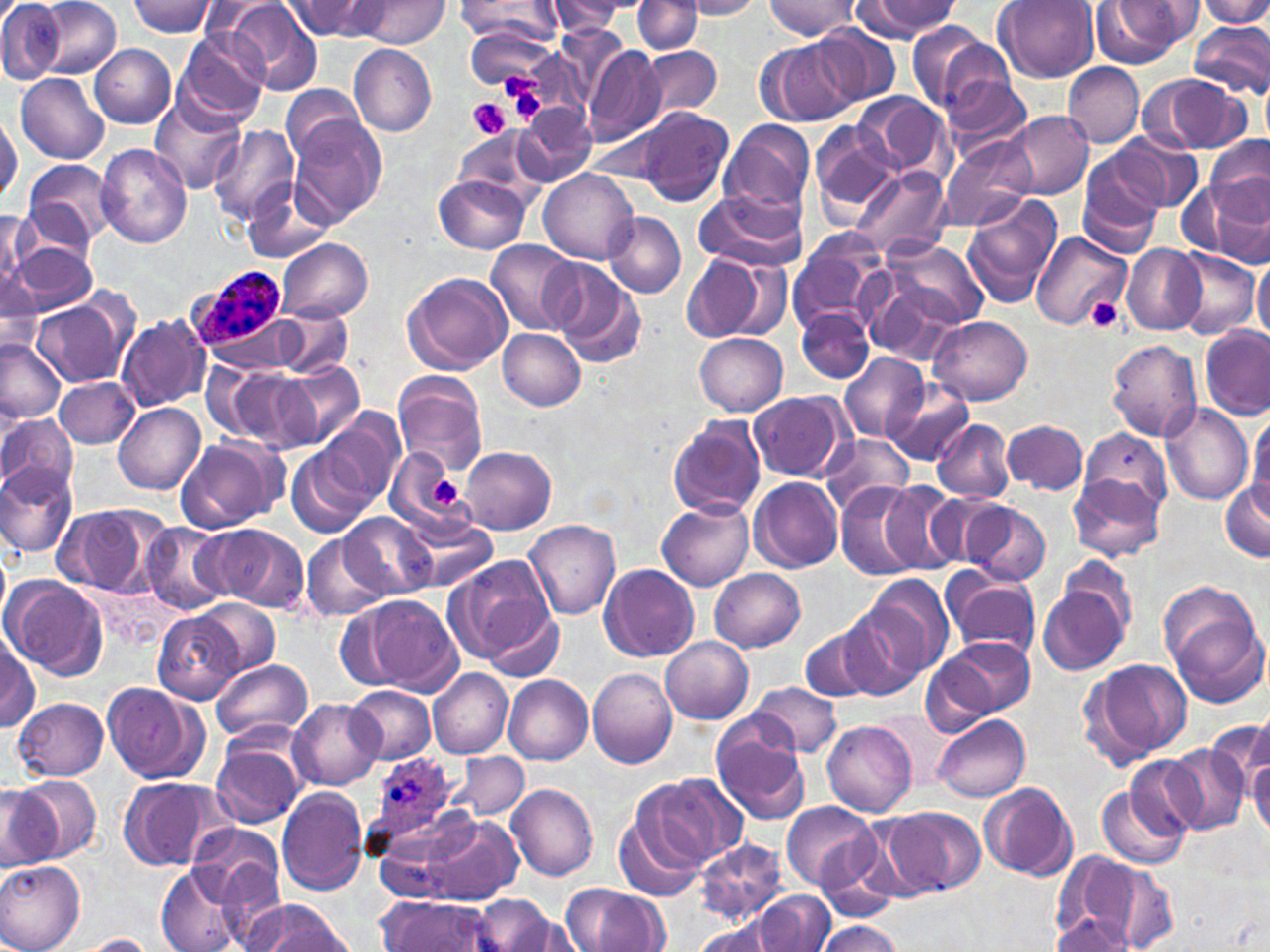 Approximate bounding boxes as named x1/y1/x2/y2 corners in pixels. Plasmodium ovale-infected red blood cell locations: (x1=191, y1=267, x2=287, y2=349), (x1=378, y1=750, x2=462, y2=838). Uninfected red blood cell locations: (x1=0, y1=0, x2=62, y2=84), (x1=34, y1=0, x2=121, y2=80), (x1=285, y1=0, x2=383, y2=39), (x1=358, y1=0, x2=446, y2=47), (x1=457, y1=0, x2=562, y2=41), (x1=683, y1=0, x2=764, y2=20), (x1=855, y1=0, x2=962, y2=39), (x1=1200, y1=0, x2=1270, y2=28), (x1=126, y1=1, x2=218, y2=37), (x1=196, y1=1, x2=287, y2=45), (x1=222, y1=1, x2=322, y2=94), (x1=548, y1=1, x2=630, y2=35), (x1=633, y1=1, x2=702, y2=55), (x1=763, y1=1, x2=860, y2=39), (x1=995, y1=1, x2=1100, y2=83), (x1=1096, y1=1, x2=1198, y2=66), (x1=1188, y1=22, x2=1270, y2=101), (x1=808, y1=25, x2=898, y2=109), (x1=906, y1=26, x2=1008, y2=120), (x1=174, y1=30, x2=269, y2=125), (x1=757, y1=39, x2=855, y2=126), (x1=90, y1=43, x2=176, y2=129), (x1=349, y1=44, x2=437, y2=138), (x1=641, y1=45, x2=721, y2=121), (x1=584, y1=46, x2=667, y2=146), (x1=1062, y1=63, x2=1145, y2=148), (x1=15, y1=73, x2=109, y2=163), (x1=939, y1=73, x2=1035, y2=161), (x1=1141, y1=73, x2=1252, y2=155), (x1=1260, y1=82, x2=1270, y2=149), (x1=283, y1=87, x2=373, y2=167), (x1=854, y1=92, x2=953, y2=182), (x1=151, y1=93, x2=246, y2=195), (x1=515, y1=104, x2=597, y2=185), (x1=637, y1=108, x2=734, y2=207), (x1=1007, y1=111, x2=1094, y2=199), (x1=1, y1=113, x2=21, y2=204), (x1=287, y1=116, x2=388, y2=227), (x1=721, y1=120, x2=816, y2=216), (x1=808, y1=121, x2=902, y2=218), (x1=210, y1=124, x2=300, y2=226), (x1=454, y1=129, x2=545, y2=201), (x1=1105, y1=132, x2=1203, y2=214), (x1=937, y1=134, x2=1037, y2=233), (x1=1206, y1=136, x2=1270, y2=217), (x1=96, y1=143, x2=192, y2=248), (x1=1076, y1=152, x2=1167, y2=257), (x1=22, y1=158, x2=117, y2=249), (x1=851, y1=166, x2=951, y2=262), (x1=540, y1=170, x2=639, y2=264), (x1=433, y1=176, x2=530, y2=253), (x1=1181, y1=177, x2=1270, y2=262), (x1=242, y1=180, x2=335, y2=265), (x1=694, y1=188, x2=805, y2=272), (x1=962, y1=196, x2=1061, y2=310), (x1=2, y1=209, x2=36, y2=291), (x1=603, y1=213, x2=685, y2=298), (x1=1030, y1=232, x2=1132, y2=330), (x1=786, y1=236, x2=889, y2=336), (x1=878, y1=238, x2=988, y2=330), (x1=277, y1=239, x2=372, y2=323), (x1=487, y1=240, x2=579, y2=334), (x1=13, y1=241, x2=95, y2=313), (x1=1121, y1=245, x2=1207, y2=335), (x1=681, y1=249, x2=792, y2=344), (x1=1170, y1=249, x2=1261, y2=339), (x1=1252, y1=254, x2=1270, y2=344), (x1=547, y1=261, x2=646, y2=367), (x1=1, y1=269, x2=45, y2=354), (x1=858, y1=271, x2=967, y2=367), (x1=402, y1=272, x2=512, y2=374), (x1=35, y1=296, x2=132, y2=387), (x1=276, y1=308, x2=352, y2=378), (x1=798, y1=308, x2=874, y2=383), (x1=116, y1=314, x2=211, y2=413), (x1=930, y1=315, x2=1033, y2=405), (x1=1200, y1=327, x2=1269, y2=420), (x1=498, y1=328, x2=586, y2=410), (x1=695, y1=332, x2=789, y2=416), (x1=1107, y1=339, x2=1202, y2=440), (x1=0, y1=340, x2=67, y2=424), (x1=838, y1=352, x2=927, y2=443), (x1=281, y1=360, x2=364, y2=449), (x1=201, y1=361, x2=277, y2=441), (x1=223, y1=369, x2=317, y2=454), (x1=393, y1=372, x2=487, y2=474), (x1=55, y1=377, x2=139, y2=450), (x1=882, y1=377, x2=974, y2=466), (x1=748, y1=391, x2=849, y2=483), (x1=113, y1=402, x2=206, y2=493), (x1=1159, y1=403, x2=1254, y2=505), (x1=319, y1=410, x2=403, y2=510), (x1=1248, y1=411, x2=1270, y2=517), (x1=0, y1=415, x2=79, y2=498), (x1=666, y1=416, x2=767, y2=519), (x1=932, y1=418, x2=1014, y2=501), (x1=1003, y1=419, x2=1088, y2=495), (x1=1078, y1=429, x2=1172, y2=519), (x1=819, y1=436, x2=914, y2=515), (x1=173, y1=437, x2=284, y2=534), (x1=460, y1=446, x2=557, y2=534), (x1=385, y1=447, x2=477, y2=541), (x1=287, y1=449, x2=368, y2=540), (x1=0, y1=464, x2=76, y2=557), (x1=1069, y1=474, x2=1166, y2=563), (x1=749, y1=478, x2=844, y2=573), (x1=1218, y1=479, x2=1270, y2=563), (x1=875, y1=482, x2=964, y2=575), (x1=836, y1=485, x2=930, y2=580), (x1=927, y1=492, x2=1022, y2=568), (x1=960, y1=500, x2=1051, y2=585), (x1=657, y1=501, x2=754, y2=590), (x1=53, y1=504, x2=164, y2=598), (x1=342, y1=513, x2=435, y2=600), (x1=402, y1=515, x2=496, y2=593), (x1=523, y1=520, x2=621, y2=618), (x1=142, y1=523, x2=230, y2=614), (x1=203, y1=523, x2=308, y2=613), (x1=300, y1=533, x2=386, y2=623), (x1=0, y1=544, x2=10, y2=623), (x1=442, y1=555, x2=559, y2=669), (x1=600, y1=565, x2=699, y2=661), (x1=710, y1=568, x2=805, y2=653), (x1=938, y1=571, x2=1041, y2=659), (x1=858, y1=573, x2=954, y2=682), (x1=2, y1=575, x2=108, y2=679), (x1=1038, y1=577, x2=1131, y2=676), (x1=1159, y1=586, x2=1268, y2=707), (x1=345, y1=595, x2=461, y2=694), (x1=192, y1=599, x2=279, y2=678), (x1=820, y1=605, x2=927, y2=702), (x1=156, y1=613, x2=242, y2=705), (x1=800, y1=623, x2=889, y2=703), (x1=1, y1=633, x2=39, y2=733), (x1=660, y1=636, x2=752, y2=723), (x1=936, y1=636, x2=1036, y2=719), (x1=920, y1=650, x2=994, y2=736), (x1=1081, y1=656, x2=1193, y2=768), (x1=209, y1=657, x2=313, y2=743), (x1=427, y1=667, x2=512, y2=758), (x1=588, y1=669, x2=677, y2=769), (x1=504, y1=675, x2=592, y2=764), (x1=102, y1=681, x2=208, y2=783), (x1=749, y1=682, x2=843, y2=759), (x1=346, y1=685, x2=435, y2=762), (x1=14, y1=697, x2=110, y2=780), (x1=288, y1=698, x2=382, y2=791), (x1=1227, y1=713, x2=1269, y2=798), (x1=931, y1=714, x2=1031, y2=801), (x1=712, y1=717, x2=811, y2=826), (x1=821, y1=718, x2=917, y2=818), (x1=1241, y1=726, x2=1270, y2=828), (x1=211, y1=735, x2=307, y2=828), (x1=1161, y1=746, x2=1249, y2=835), (x1=450, y1=752, x2=528, y2=819), (x1=1249, y1=757, x2=1270, y2=840), (x1=1127, y1=758, x2=1209, y2=844), (x1=15, y1=774, x2=101, y2=861), (x1=645, y1=774, x2=744, y2=868), (x1=118, y1=777, x2=229, y2=872), (x1=1098, y1=779, x2=1189, y2=869), (x1=505, y1=782, x2=599, y2=882), (x1=978, y1=782, x2=1077, y2=881), (x1=0, y1=786, x2=58, y2=873), (x1=275, y1=788, x2=368, y2=896), (x1=781, y1=800, x2=878, y2=893), (x1=615, y1=802, x2=710, y2=903), (x1=885, y1=807, x2=984, y2=896), (x1=399, y1=811, x2=524, y2=906), (x1=187, y1=822, x2=284, y2=910), (x1=697, y1=838, x2=790, y2=925), (x1=1077, y1=856, x2=1178, y2=949), (x1=0, y1=861, x2=86, y2=952), (x1=156, y1=867, x2=246, y2=952), (x1=562, y1=884, x2=669, y2=952), (x1=752, y1=892, x2=833, y2=952), (x1=378, y1=895, x2=492, y2=952), (x1=474, y1=895, x2=566, y2=952), (x1=242, y1=901, x2=351, y2=952), (x1=1051, y1=912, x2=1136, y2=950), (x1=696, y1=917, x2=793, y2=952), (x1=818, y1=920, x2=903, y2=951), (x1=77, y1=934, x2=159, y2=951). Platelet locations: (x1=504, y1=79, x2=548, y2=129), (x1=469, y1=98, x2=511, y2=141), (x1=1083, y1=297, x2=1125, y2=331), (x1=432, y1=477, x2=461, y2=507). Slide-level diagnosis: Plasmodium ovale. Single field of view. 1000x magnification. Light microscopy. Image is 1270×952 pixels. May-Grünwald-Giemsa-stained preparation. Thin blood smear.